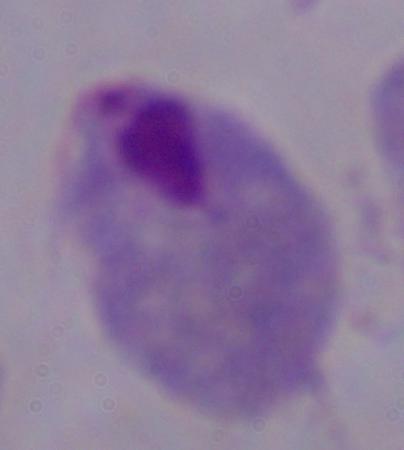
{
  "identification": "trichomonad",
  "magnification": "1000x",
  "modality": "micrograph"
}